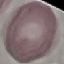

malaria_status: uninfected
preparation: thin blood smear
stain: Giemsa
image_type: cell patch, automatically extracted from a larger field of view and resized to 64 × 64 pixels
capture: smartphone through the microscope eyepiece